Outline each blood parasite and name the species.
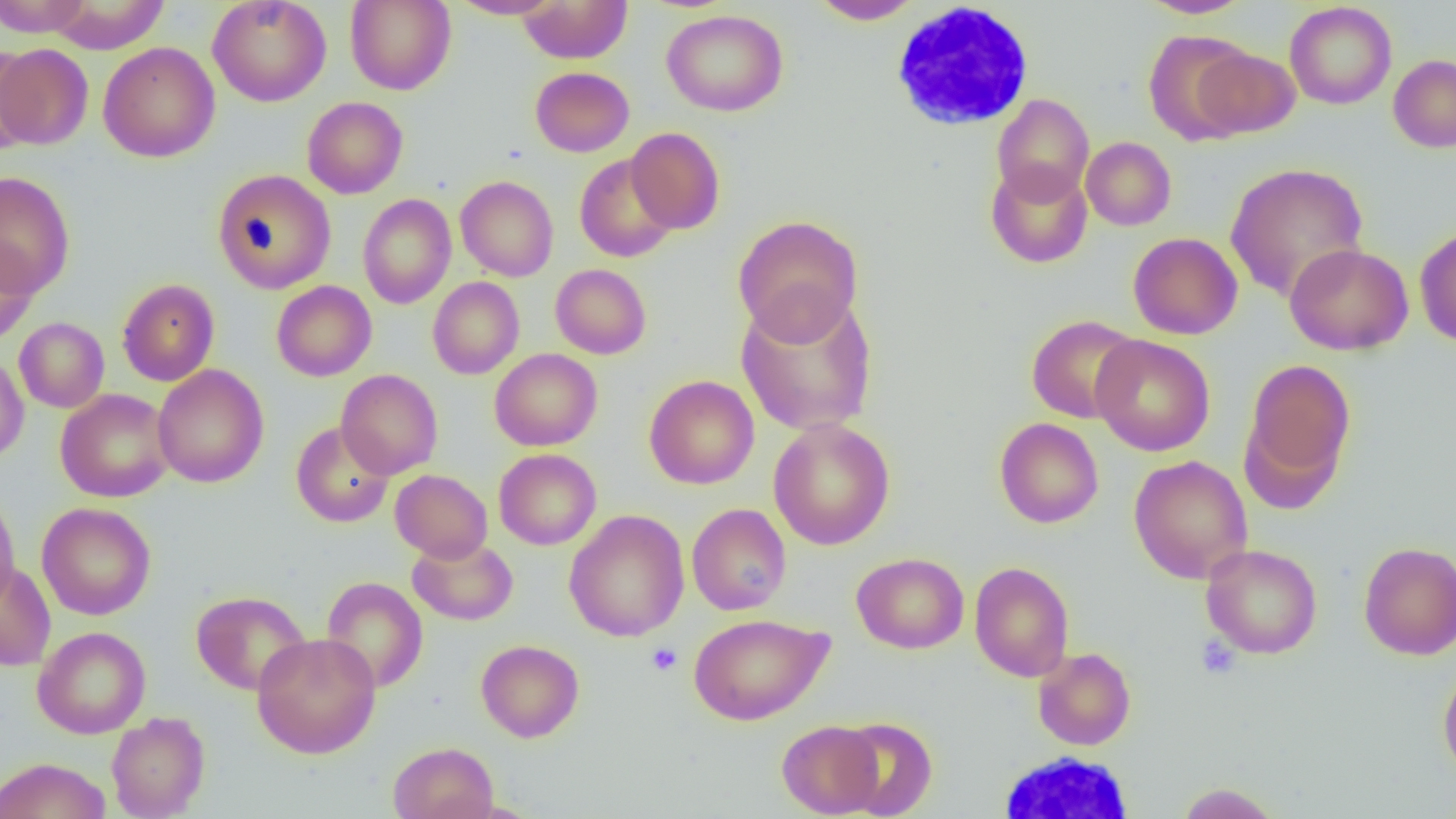

No blood parasites observed.

slide-level diagnosis = no evidence of blood parasites
uninfected red blood cell locations = approximate bounding boxes as (x1, y1, x2, y2) in pixels: (0, 0, 92, 37), (45, 0, 169, 54), (207, 0, 331, 107), (449, 0, 561, 19), (808, 0, 924, 25), (1139, 0, 1252, 19), (345, 1, 456, 95), (517, 1, 633, 64), (1284, 2, 1397, 109), (661, 10, 788, 116), (1142, 29, 1257, 145), (98, 42, 220, 162), (0, 44, 94, 149), (0, 44, 43, 156), (1193, 47, 1300, 138), (1388, 55, 1456, 152), (530, 66, 634, 157), (992, 93, 1094, 204), (302, 96, 408, 199), (625, 127, 726, 234), (1081, 137, 1176, 230), (574, 154, 680, 263), (985, 161, 1093, 268), (1225, 162, 1369, 302), (212, 168, 336, 294), (0, 171, 75, 297), (456, 176, 558, 282), (357, 193, 456, 309), (733, 214, 864, 343), (1415, 226, 1456, 347), (1128, 232, 1243, 340), (0, 236, 39, 347), (1285, 243, 1413, 355), (550, 264, 651, 359), (427, 277, 524, 379), (117, 278, 220, 386), (271, 280, 377, 381), (736, 292, 879, 436), (1026, 315, 1142, 423), (14, 317, 109, 413), (1091, 333, 1216, 456), (490, 348, 602, 451), (0, 353, 29, 464), (1241, 358, 1356, 497), (152, 364, 269, 488), (336, 369, 443, 479), (644, 374, 759, 489), (55, 388, 174, 502), (994, 417, 1103, 528), (768, 418, 895, 550), (291, 422, 395, 527), (494, 449, 601, 550), (1129, 455, 1253, 584), (390, 469, 493, 562), (0, 489, 20, 611), (37, 502, 156, 620), (686, 503, 791, 615), (564, 509, 689, 642), (407, 536, 518, 626), (1358, 541, 1456, 660), (1201, 543, 1322, 659), (852, 552, 969, 654), (0, 560, 56, 671), (970, 561, 1074, 681), (321, 576, 429, 693), (191, 590, 311, 695), (689, 613, 833, 725), (33, 626, 151, 738), (252, 632, 381, 758), (476, 639, 584, 742), (1033, 647, 1136, 750), (1438, 663, 1456, 780), (106, 711, 210, 818), (837, 717, 938, 818), (777, 719, 884, 817), (388, 741, 499, 819), (0, 757, 111, 819), (1176, 782, 1281, 818)
magnification = 1000x
preparation = thin blood smear
platelet locations = approximate bounding boxes as (x1, y1, x2, y2) in pixels: (1196, 635, 1241, 679), (646, 642, 682, 675)
field of view = single
image size = 1456×819 pixels
modality = optical microscopy
white blood cell locations = approximate bounding boxes as (x1, y1, x2, y2) in pixels: (889, 2, 1036, 132), (993, 751, 1140, 817)